Look for Plasmodium parasites.
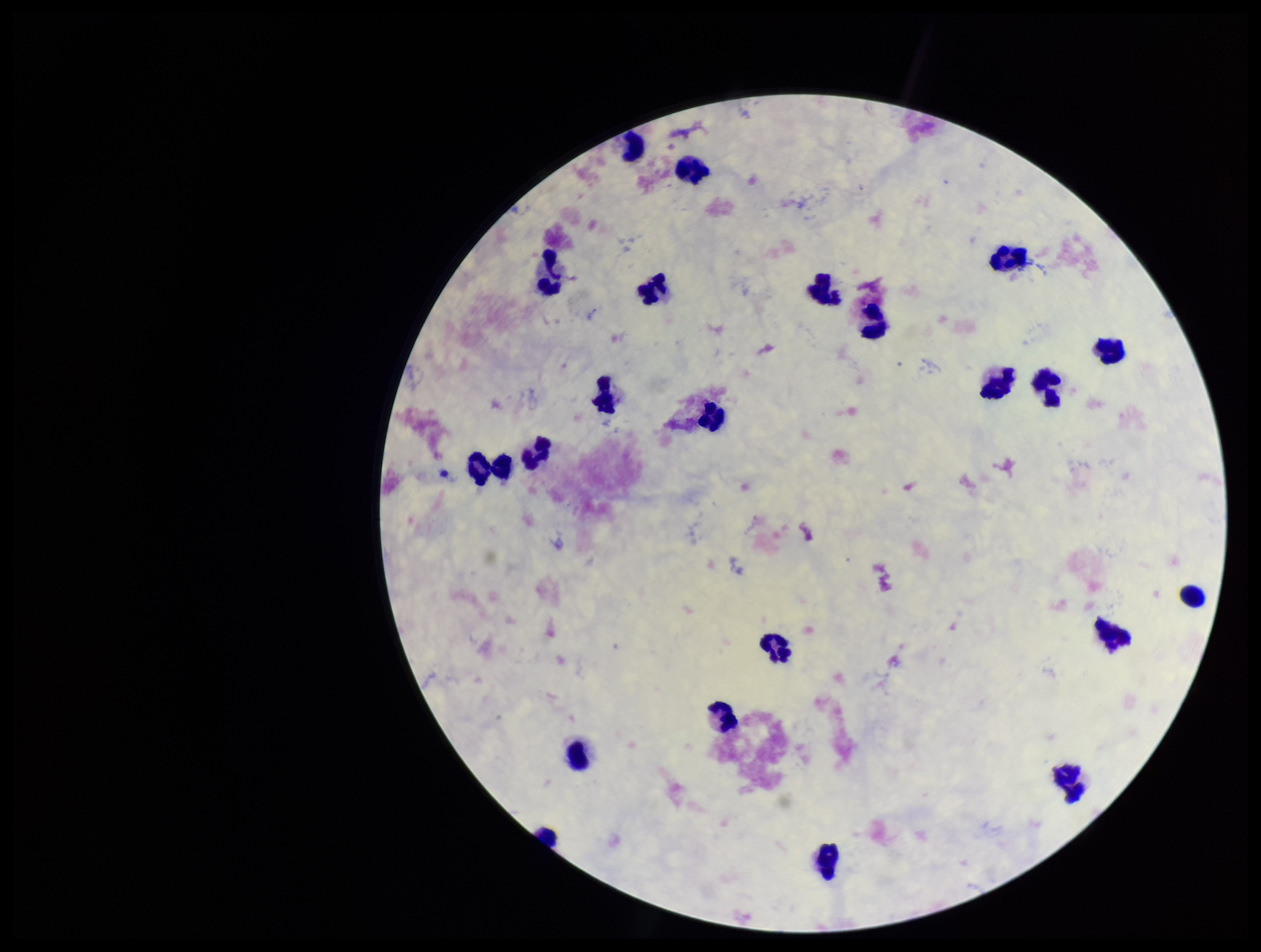

None identified.

Summary:
  - Leukocyte count: 22
  - Field of view: one from this slide
  - Preparation: thick
  - Capture: smartphone photograph through the microscope eyepiece
  - Parasite count: 0
  - Patient malaria status: negative
  - Stain: Giemsa
  - Image size: 1261×952 pixels